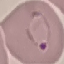 Malaria status: parasitized. Photographed with a smartphone camera at the microscope eyepiece. Cell patch, automatically extracted from a larger field of view and resized to 64 × 64 pixels. Giemsa stain. Thin smear of blood.